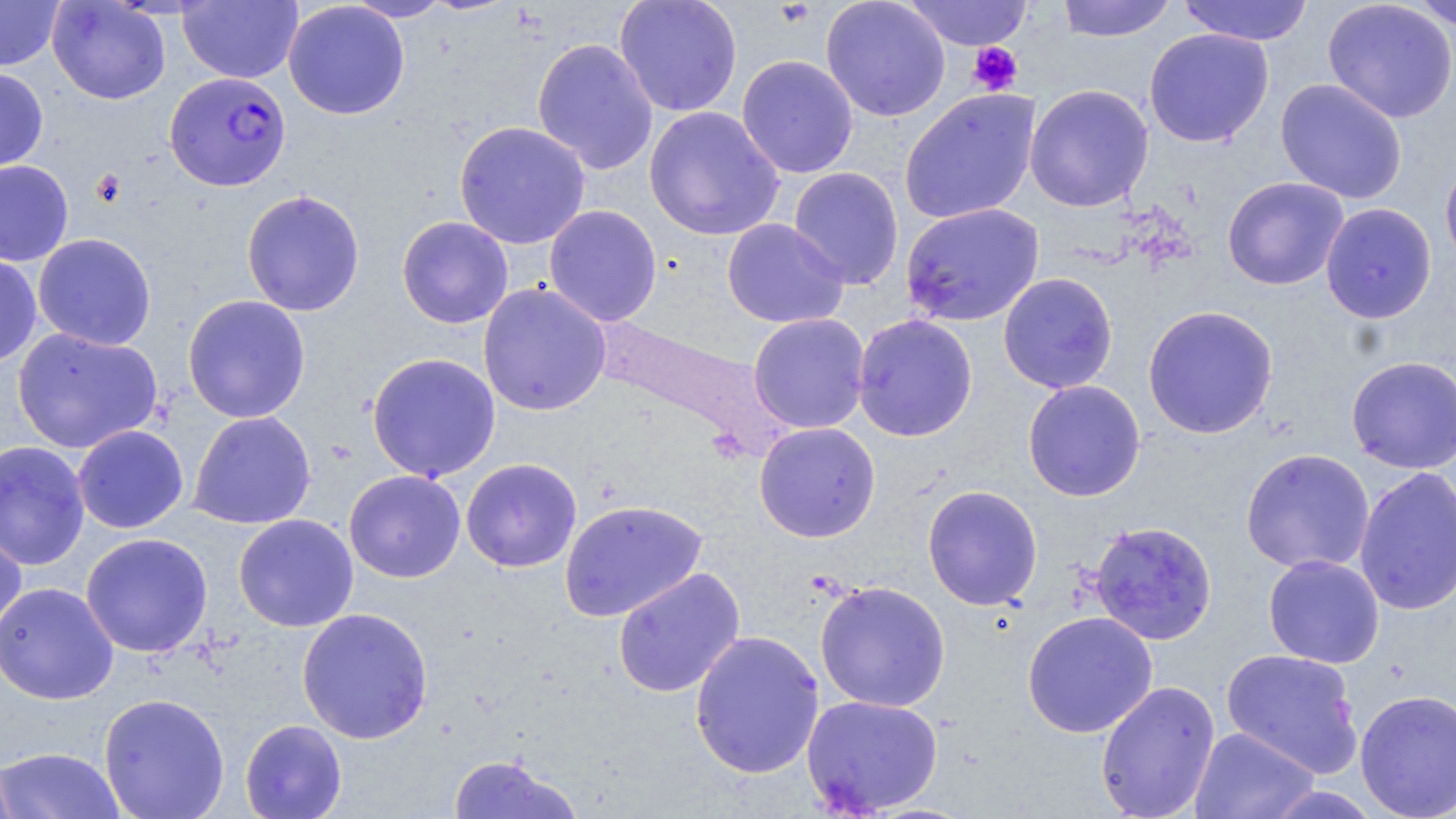 Approximate bounding boxes as [x1, y1, x2, y2] in pixels. Plasmodium falciparum-infected red blood cell locations: [164, 71, 291, 192]. Uninfected red blood cell locations: [0, 0, 65, 71], [47, 0, 171, 105], [178, 0, 303, 83], [344, 0, 453, 22], [614, 0, 743, 117], [820, 0, 950, 122], [903, 0, 1034, 51], [1056, 0, 1176, 42], [1177, 0, 1313, 46], [1322, 0, 1456, 124], [1405, 0, 1456, 31], [283, 1, 410, 120], [1144, 28, 1274, 148], [532, 37, 659, 175], [736, 54, 859, 178], [0, 68, 49, 175], [1275, 78, 1408, 204], [1024, 84, 1154, 212], [899, 88, 1041, 225], [644, 105, 784, 241], [453, 120, 591, 249], [1440, 154, 1456, 273], [0, 160, 74, 266], [788, 166, 904, 289], [1222, 176, 1349, 291], [241, 189, 365, 317], [900, 202, 1044, 327], [1320, 203, 1437, 323], [544, 204, 662, 327], [396, 216, 514, 329], [721, 218, 850, 329], [33, 233, 157, 351], [0, 252, 42, 368], [997, 272, 1119, 394], [478, 281, 611, 417], [182, 294, 311, 423], [1142, 304, 1279, 439], [748, 313, 870, 433], [852, 314, 978, 441], [12, 327, 163, 454], [366, 352, 501, 482], [1346, 356, 1456, 473], [1022, 379, 1145, 502], [188, 410, 317, 529], [754, 421, 881, 542], [72, 425, 189, 533], [0, 440, 91, 571], [1241, 448, 1375, 574], [461, 458, 582, 572], [1354, 465, 1456, 615], [344, 469, 466, 583], [922, 484, 1043, 610], [559, 499, 708, 622], [233, 514, 359, 632], [1088, 520, 1218, 645], [0, 523, 27, 644], [80, 532, 213, 658], [1263, 554, 1385, 668], [612, 567, 746, 698], [814, 580, 951, 713], [0, 581, 119, 705], [296, 607, 434, 744], [1022, 611, 1158, 738], [689, 630, 825, 779], [1221, 648, 1363, 777], [1095, 680, 1221, 819], [1354, 688, 1456, 819], [98, 693, 230, 819], [801, 694, 944, 815], [240, 719, 347, 819], [1190, 726, 1319, 819], [0, 746, 126, 819], [447, 754, 581, 818], [0, 756, 19, 819]. Platelet locations: [968, 42, 1022, 96]. Slide-level diagnosis: Plasmodium falciparum. May-Grünwald-Giemsa-stained preparation. Thin blood smear. Light microscopy. Image is 1456×819 pixels. Captured at 1000x magnification. One field of a larger specimen.